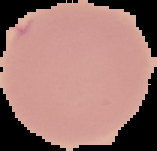
Summary:
  - Image type: cell region segmented out of the field of view; surrounding area masked to black
  - Preparation: thin blood smear
  - Image size: 157×151 pixels
  - Result: no Plasmodium parasites seen